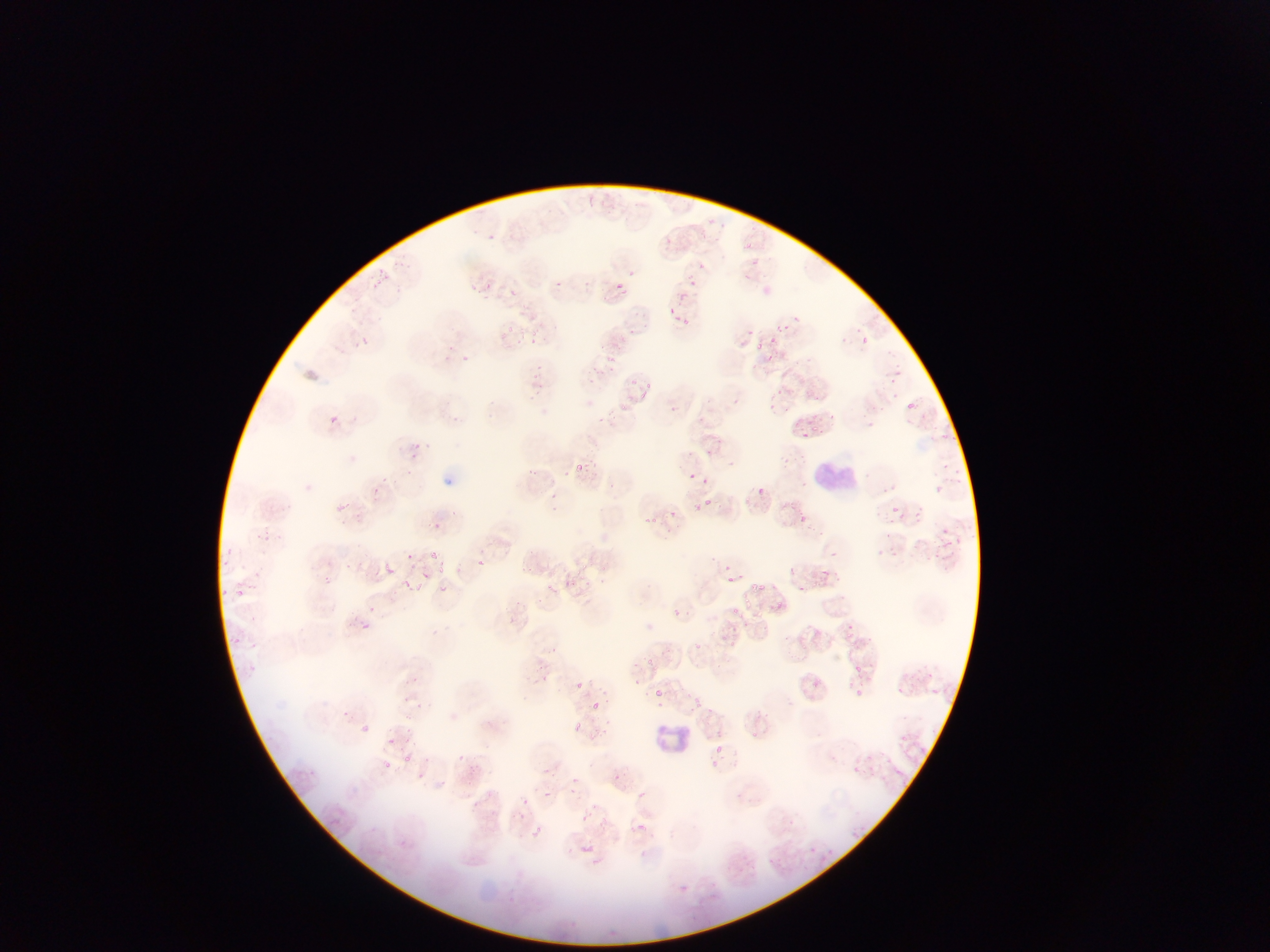

capture: mobile-phone photograph through a microscope
field_of_view: single
image_size: 1270×952 pixels
preparation: thin blood smear
country: Ghana
leukocyte_locations: 'approximate bounding boxes as left top right bottom in pixels: 813 456 861 501; 650 717 697 760'
malaria_parasite_locations: 'approximate bounding boxes as left top right bottom in pixels: 485 229 501 243; 473 231 483 244; 742 241 753 251; 697 261 708 271; 379 266 392 281; 625 271 636 283; 738 272 747 283; 688 273 693 288; 548 277 566 291; 614 280 625 293; 485 284 494 292; 678 285 695 308; 512 288 529 305; 667 304 680 323; 793 311 800 323; 683 315 691 326; 780 321 789 336; 507 324 517 337; 528 324 537 339; 748 328 758 341; 358 336 370 347; 859 336 869 345; 768 337 777 343; 599 338 610 354; 754 341 770 356; 450 342 459 352; 458 353 472 363; 608 353 619 361; 443 356 452 366; 896 360 908 369; 533 364 546 376; 597 371 601 380; 890 372 906 385; 630 373 639 383; 646 381 657 389; 770 385 780 397; 640 389 650 401; 731 391 749 409; 621 398 631 413; 878 398 895 415; 905 398 917 415; 664 405 676 417; 783 405 793 418; 767 407 781 423; 829 411 841 423; 328 415 340 425; 867 417 878 432; 812 425 823 437; 797 429 807 444; 936 429 947 441; 952 432 961 444; 412 439 422 453; 705 441 711 453; 729 456 738 468; 784 456 793 463; 574 461 583 471; 942 463 954 480; 531 465 542 477; 686 467 698 484; 800 476 813 493; 699 478 712 489; 934 483 945 494; 758 485 773 501; 371 487 387 501; 550 489 562 501; 343 495 356 514; 700 498 709 511; 913 504 925 522; 670 507 678 525; 889 507 900 519; 643 513 654 528; 797 514 811 527; 436 522 442 534; 943 528 958 543; 884 530 893 541; 255 533 268 545; 426 542 443 560; 221 544 236 556; 408 548 419 564; 832 548 842 564; 933 551 946 566; 222 559 232 569; 471 559 491 577; 346 561 358 574; 384 561 392 572; 727 561 738 576; 438 563 449 576; 580 563 592 574; 787 566 796 575; 252 567 265 578; 821 570 836 583; 421 571 430 579; 326 574 338 590; 564 574 575 586; 575 575 595 591; 727 575 741 586; 402 579 415 590; 751 581 765 593; 438 584 449 590; 796 584 807 595; 233 585 246 596; 543 586 553 601; 220 589 231 599; 720 602 746 619; 673 606 685 618; 361 619 372 633; 848 622 859 638; 230 634 246 644; 731 638 743 650; 690 641 705 649; 547 645 558 651; 250 656 266 678; 645 656 661 671; 855 664 868 675; 919 670 940 680; 810 675 825 690; 410 677 428 684; 574 681 584 691; 680 683 689 694; 852 687 862 697; 650 689 665 702; 692 694 703 706; 398 696 416 706; 585 700 605 710; 417 702 426 711; 710 707 721 719; 362 722 378 737; 572 722 583 733; 751 730 766 741; 896 732 911 748; 389 736 395 744; 716 743 724 751; 863 752 875 764; 402 755 413 764; 378 756 397 775; 711 757 725 770; 544 765 555 782; 854 765 864 776; 417 766 421 782; 609 770 624 786; 572 788 578 801; 543 792 552 801; 523 798 535 813; 577 814 588 827; 637 821 649 835; 530 826 548 837; 810 846 819 855; 680 884 689 894 | approximate x y pixel centers of objects too small to bound: 473 285; 373 608; 409 727; 409 740'